Report the malaria status of this cell.
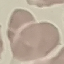

It is uninfected.

{
  "stain": "Giemsa",
  "preparation": "thin smear",
  "image_type": "cell patch, automatically extracted from a larger field of view and resized to 64 × 64 pixels",
  "capture": "smartphone through the microscope eyepiece"
}